Assess the morphology of the erythrocytes.
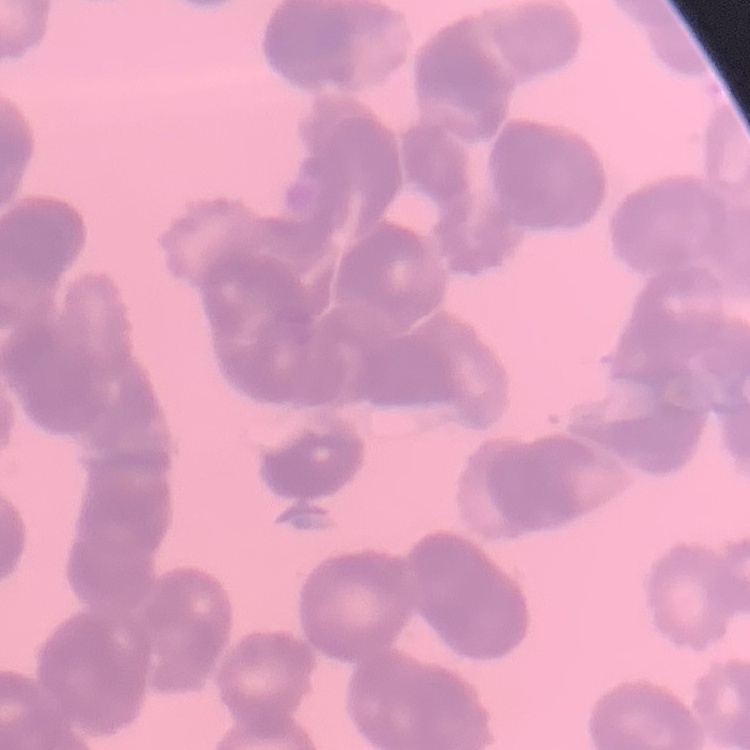

Rouleaux formation.

stain = Field's or Giemsa
image type = square crop of a larger photomicrograph
preparation = thin blood smear